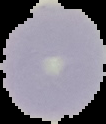
Summary:
  - Preparation: thin blood smear
  - Result: no Plasmodium parasites detected
  - Image type: segmented cell region with the area outside set to black
  - Image size: 106×124 pixels